State the blood parasite species.
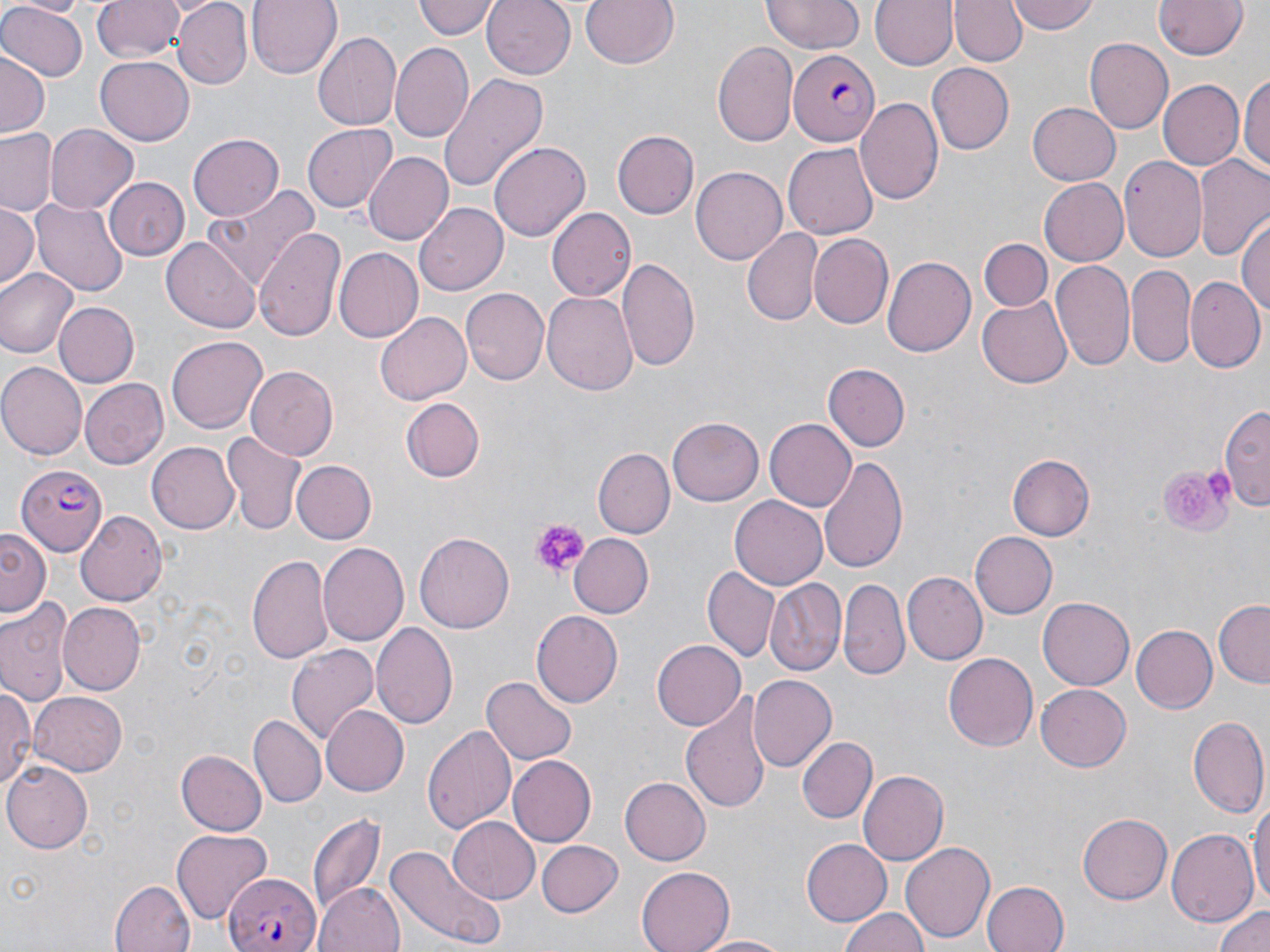
Plasmodium falciparum.

Approximate bounding boxes as (x1,y1)-(x2,y2) corner pairs in pixels. Uninfected red blood cell locations: (16,0)-(88,16), (93,0)-(187,64), (173,0)-(253,90), (248,0)-(341,77), (415,0)-(497,40), (579,0)-(677,70), (762,0)-(864,55), (870,0)-(956,71), (1008,0)-(1100,36), (1153,0)-(1249,59), (483,1)-(575,80), (951,1)-(1025,65), (0,3)-(87,83), (312,31)-(402,129), (1087,37)-(1174,134), (711,40)-(799,149), (390,43)-(474,143), (0,52)-(47,138), (96,59)-(193,144), (928,64)-(1014,154), (1240,70)-(1269,177), (440,72)-(550,190), (1157,80)-(1243,170), (854,97)-(943,208), (1027,100)-(1121,184), (302,123)-(397,215), (44,124)-(138,215), (0,129)-(60,215), (612,130)-(699,219), (187,133)-(284,220), (490,142)-(590,240), (784,142)-(878,238), (363,152)-(454,245), (1120,156)-(1209,261), (1194,157)-(1270,259), (691,167)-(786,265), (105,177)-(190,261), (1039,177)-(1127,266), (203,187)-(319,290), (31,197)-(130,297), (0,202)-(38,289), (416,203)-(509,295), (547,205)-(637,302), (1237,216)-(1270,319), (254,226)-(345,342), (743,226)-(820,324), (808,234)-(893,330), (162,238)-(258,332), (981,238)-(1053,311), (334,248)-(425,342), (881,256)-(975,358), (618,258)-(701,374), (1051,258)-(1133,372), (1127,263)-(1196,367), (0,267)-(77,358), (1186,276)-(1264,372), (461,288)-(549,387), (543,291)-(637,398), (980,298)-(1071,387), (53,302)-(138,387), (374,313)-(471,405), (168,335)-(267,433), (0,362)-(85,460), (822,363)-(910,450), (245,365)-(338,460), (80,378)-(168,468), (401,398)-(484,482), (1219,404)-(1269,507), (669,418)-(763,505), (766,418)-(859,511), (221,431)-(306,535), (147,441)-(241,535), (595,447)-(673,536), (819,453)-(909,575), (1009,454)-(1093,540), (292,461)-(376,543), (731,496)-(827,589), (75,507)-(167,603), (0,529)-(51,612), (415,531)-(514,632), (568,532)-(654,618), (971,532)-(1057,617), (317,543)-(408,646), (248,552)-(334,665), (703,566)-(780,663), (903,572)-(986,665), (839,576)-(909,679), (766,580)-(846,676), (1038,597)-(1134,690), (0,599)-(72,707), (1214,599)-(1270,689), (58,601)-(145,694), (532,611)-(623,708), (372,621)-(458,730), (1132,624)-(1217,713), (651,639)-(746,731), (287,642)-(380,744), (944,652)-(1039,751), (484,675)-(577,764), (748,675)-(836,774), (0,682)-(33,796), (1036,683)-(1131,771), (29,693)-(127,776), (682,698)-(769,817), (322,704)-(409,797), (1187,714)-(1267,817), (250,716)-(326,805), (421,722)-(515,832), (796,736)-(876,823), (176,748)-(266,834), (508,756)-(595,845), (3,763)-(92,852), (859,770)-(947,865), (619,777)-(710,865), (1250,793)-(1269,910), (309,812)-(386,914), (1078,813)-(1172,904), (449,816)-(540,903), (1166,829)-(1258,928), (172,830)-(271,921), (802,838)-(891,922), (536,839)-(625,917), (900,840)-(994,943), (389,843)-(508,948), (636,865)-(736,952), (109,879)-(194,952), (314,881)-(404,952), (980,881)-(1068,952), (1213,903)-(1270,952), (838,906)-(929,952), (696,934)-(792,952). Plasmodium falciparum-infected red blood cell locations: (788,49)-(881,145), (15,461)-(104,554), (226,872)-(325,952). Platelet locations: (1153,460)-(1235,537), (528,520)-(587,576). Captured at 1000x magnification. One field of a larger specimen. Light microscopy. Thin blood film. Image is 1270×952 pixels. May-Grünwald-Giemsa stain.